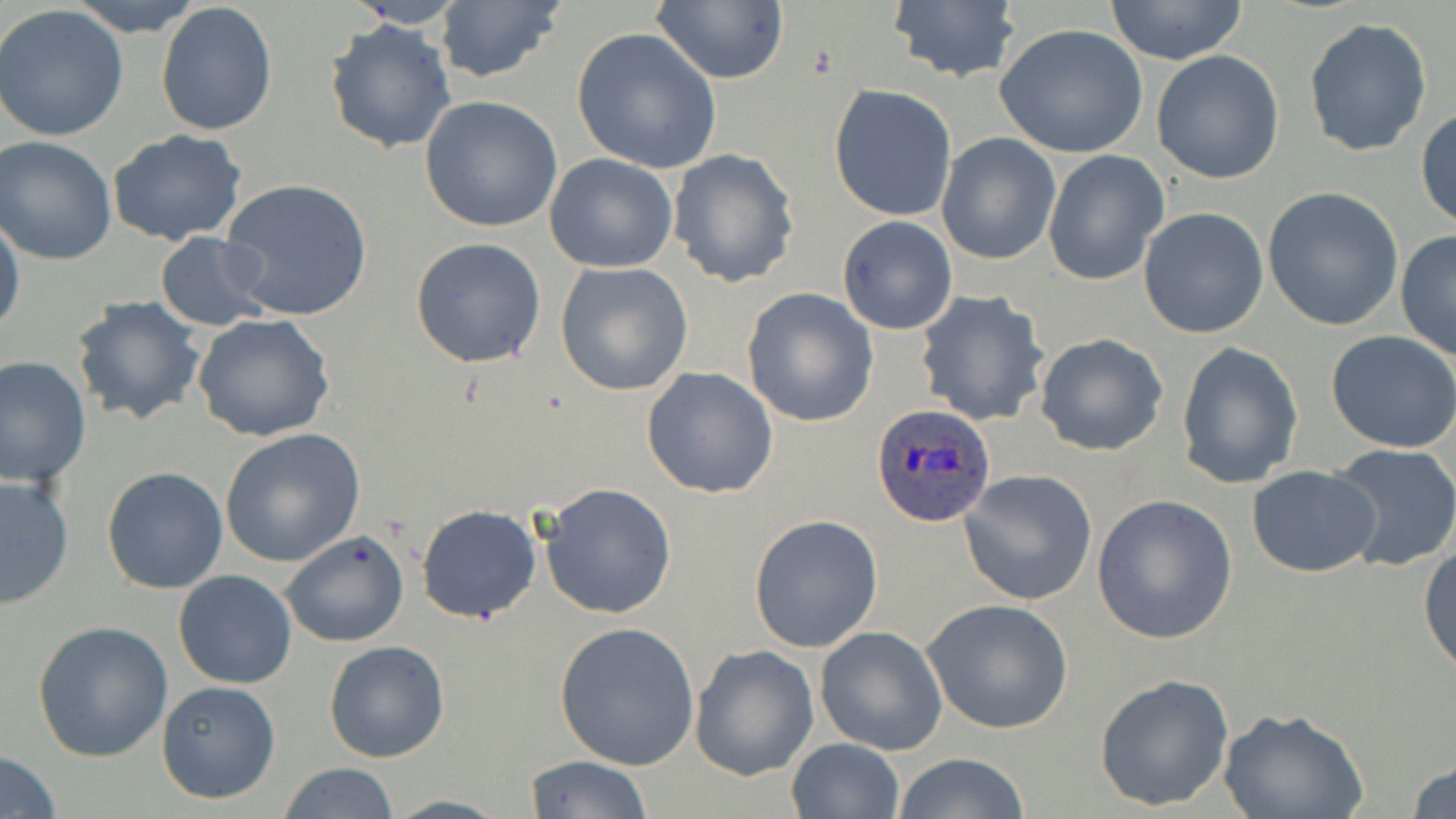
slide-level diagnosis = Plasmodium ovale
image size = 1456×819 pixels
field of view = one of a larger specimen
stain = May-Grünwald-Giemsa
Plasmodium ovale-infected red blood cell locations = approximate bounding boxes as named x1/y1/x2/y2 corners in pixels: (x1=870, y1=404, x2=996, y2=528)
preparation = thin blood film
magnification = 1000x
modality = optical microscopy
uninfected red blood cell locations = approximate bounding boxes as named x1/y1/x2/y2 corners in pixels: (x1=67, y1=0, x2=204, y2=34), (x1=651, y1=0, x2=788, y2=85), (x1=154, y1=1, x2=278, y2=138), (x1=342, y1=1, x2=469, y2=29), (x1=1105, y1=1, x2=1249, y2=65), (x1=433, y1=2, x2=565, y2=85), (x1=885, y1=2, x2=1023, y2=84), (x1=0, y1=5, x2=129, y2=143), (x1=1303, y1=17, x2=1433, y2=157), (x1=323, y1=19, x2=458, y2=156), (x1=993, y1=23, x2=1149, y2=160), (x1=570, y1=28, x2=722, y2=176), (x1=1151, y1=50, x2=1284, y2=185), (x1=828, y1=84, x2=958, y2=222), (x1=418, y1=95, x2=563, y2=234), (x1=1416, y1=105, x2=1456, y2=233), (x1=105, y1=129, x2=249, y2=247), (x1=936, y1=132, x2=1061, y2=265), (x1=1, y1=137, x2=119, y2=265), (x1=667, y1=148, x2=801, y2=288), (x1=1041, y1=150, x2=1168, y2=288), (x1=543, y1=153, x2=680, y2=274), (x1=219, y1=177, x2=373, y2=322), (x1=1263, y1=186, x2=1405, y2=333), (x1=1138, y1=207, x2=1270, y2=339), (x1=0, y1=213, x2=25, y2=343), (x1=836, y1=215, x2=959, y2=336), (x1=1395, y1=230, x2=1456, y2=362), (x1=155, y1=233, x2=272, y2=332), (x1=410, y1=237, x2=547, y2=368), (x1=554, y1=261, x2=694, y2=396), (x1=741, y1=287, x2=879, y2=429), (x1=915, y1=290, x2=1051, y2=428), (x1=69, y1=296, x2=207, y2=426), (x1=192, y1=314, x2=336, y2=443), (x1=1326, y1=330, x2=1456, y2=452), (x1=1034, y1=333, x2=1170, y2=457), (x1=1175, y1=341, x2=1304, y2=491), (x1=0, y1=356, x2=91, y2=488), (x1=641, y1=366, x2=780, y2=499), (x1=219, y1=429, x2=366, y2=567), (x1=1329, y1=444, x2=1456, y2=572), (x1=1246, y1=463, x2=1382, y2=578), (x1=102, y1=465, x2=230, y2=594), (x1=959, y1=470, x2=1098, y2=608), (x1=0, y1=472, x2=75, y2=609), (x1=539, y1=483, x2=676, y2=620), (x1=1092, y1=494, x2=1238, y2=644), (x1=416, y1=503, x2=543, y2=624), (x1=749, y1=514, x2=883, y2=653), (x1=281, y1=530, x2=409, y2=648), (x1=1418, y1=538, x2=1455, y2=676), (x1=174, y1=569, x2=297, y2=689), (x1=922, y1=598, x2=1073, y2=735), (x1=552, y1=620, x2=702, y2=769), (x1=33, y1=621, x2=173, y2=762), (x1=815, y1=626, x2=948, y2=755), (x1=322, y1=639, x2=450, y2=763), (x1=689, y1=645, x2=818, y2=781), (x1=1093, y1=672, x2=1236, y2=812), (x1=155, y1=680, x2=282, y2=804), (x1=1221, y1=710, x2=1366, y2=819), (x1=785, y1=737, x2=906, y2=819), (x1=0, y1=750, x2=61, y2=817), (x1=894, y1=753, x2=1031, y2=818), (x1=525, y1=754, x2=654, y2=818), (x1=1408, y1=757, x2=1456, y2=819), (x1=277, y1=762, x2=401, y2=818), (x1=380, y1=794, x2=515, y2=818)